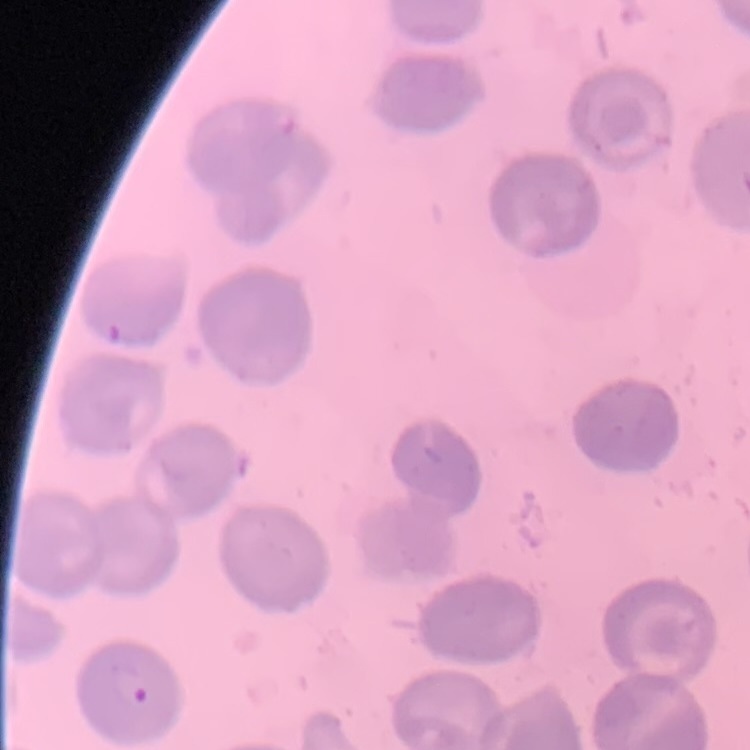

{
  "red_blood_cell_morphology": "no rouleaux formation",
  "stain": "Field's or Giemsa",
  "image_type": "one tile cut from a larger photomicrograph",
  "preparation": "thin blood film"
}